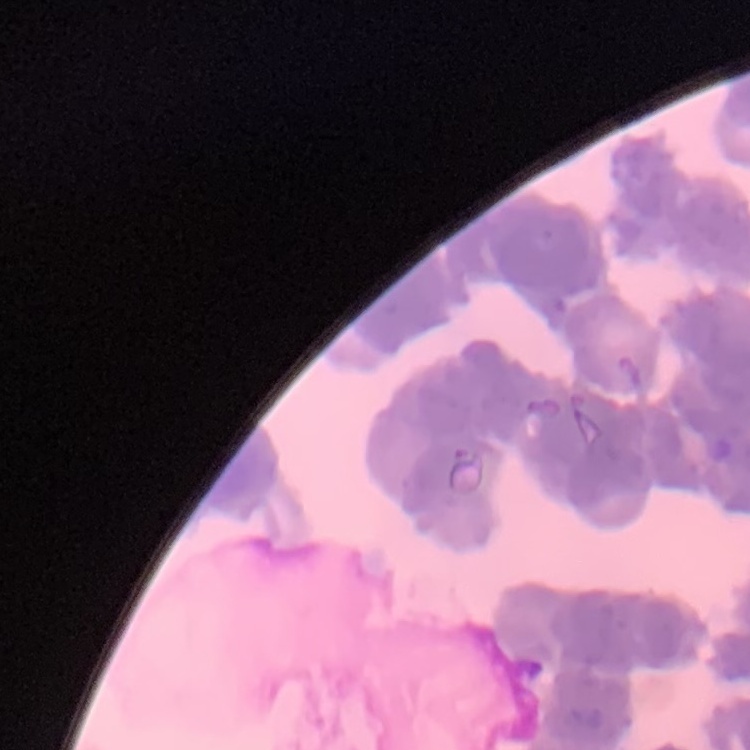
The red blood cells exhibit rouleaux formation. Stained with either Field's or Giemsa. Square crop of a larger photomicrograph. Thin blood smear.